Report the malaria status of this cell.
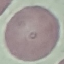

Uninfected.

capture = smartphone camera at the microscope eyepiece
image type = cell patch, automatically extracted from a larger field of view and resized to 64 × 64 pixels
preparation = thin blood smear
stain = Giemsa